Outline each Plasmodium falciparum-infected red blood cell.
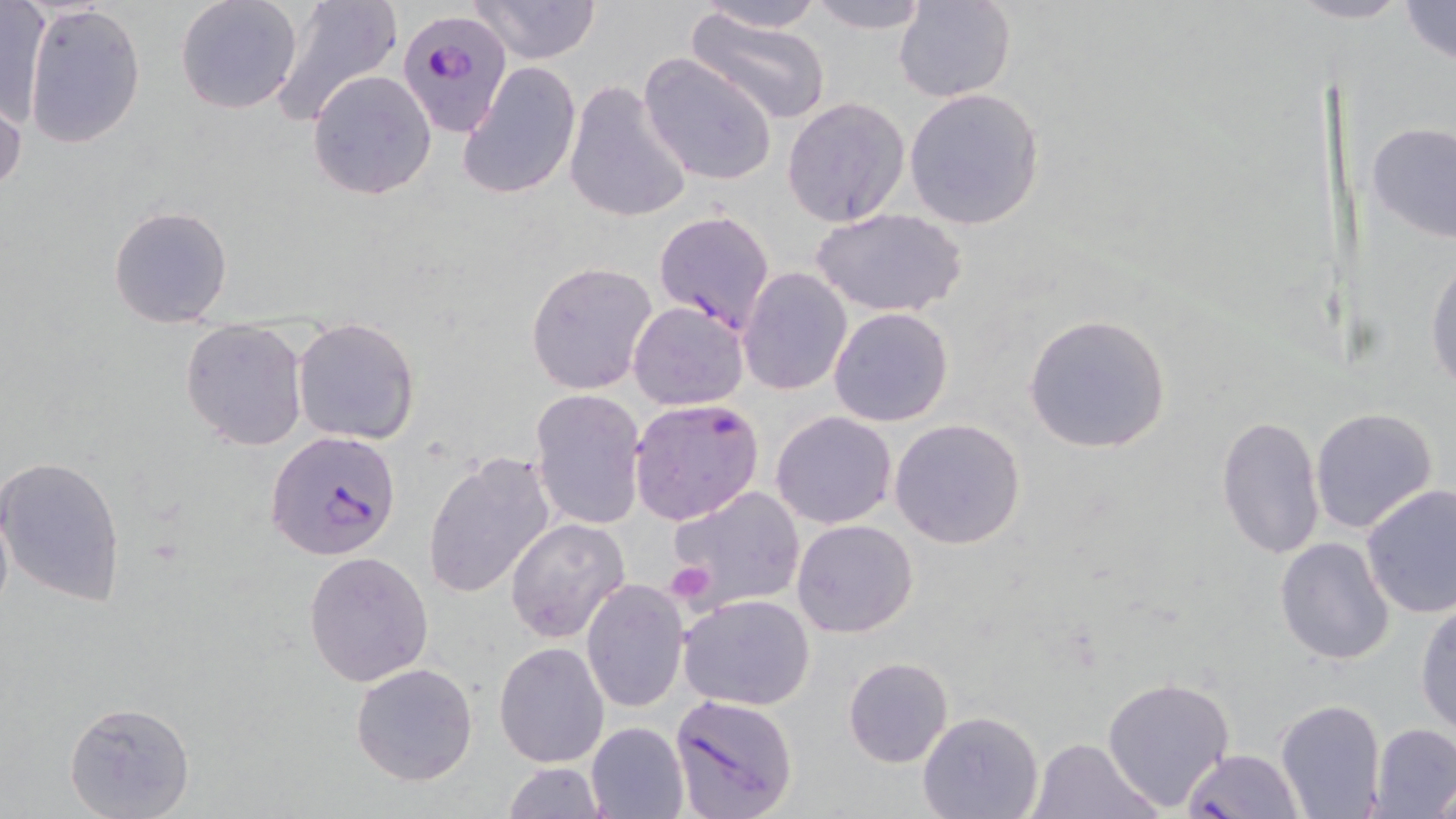

Approximate bounding boxes as (x1,y1)-(x2,y2) corner pairs in pixels.
Plasmodium falciparum-infected red blood cells: (398,5)-(513,134), (628,398)-(764,525), (266,430)-(401,561), (668,694)-(799,817), (1180,748)-(1305,819).

Summary:
  - Uninfected red blood cell locations: (1,0)-(48,128), (175,0)-(303,114), (474,0)-(600,63), (803,0)-(933,32), (895,0)-(1016,102), (1396,0)-(1455,67), (267,1)-(403,126), (691,1)-(829,34), (23,2)-(145,149), (685,10)-(833,128), (638,52)-(779,187), (457,60)-(582,201), (307,70)-(437,199), (564,80)-(693,225), (903,88)-(1044,230), (0,93)-(24,199), (782,96)-(910,227), (1366,121)-(1456,243), (108,204)-(234,329), (811,208)-(968,317), (654,209)-(775,331), (1425,250)-(1456,395), (526,261)-(656,394), (739,267)-(852,395), (629,302)-(749,411), (828,307)-(954,427), (1022,313)-(1173,455), (292,318)-(420,445), (180,320)-(307,451), (530,388)-(647,530), (1308,407)-(1438,534), (771,410)-(897,529), (1215,415)-(1326,560), (888,418)-(1027,550), (423,453)-(555,600), (0,454)-(127,605), (1360,484)-(1456,618), (669,486)-(806,609), (0,489)-(14,632), (506,516)-(631,644), (792,519)-(918,637), (1275,536)-(1394,665), (304,550)-(435,687), (581,580)-(689,713), (679,594)-(815,710), (1415,598)-(1456,737), (494,642)-(609,768), (843,657)-(952,767), (351,663)-(479,785), (1101,675)-(1236,811), (1274,699)-(1387,819), (64,700)-(195,818), (917,711)-(1042,818), (587,721)-(690,819), (1369,723)-(1455,817), (1027,736)-(1161,819), (500,762)-(607,819), (1427,778)-(1456,816)
  - Platelet locations: (666,562)-(719,607)
  - Slide-level diagnosis: Plasmodium falciparum
  - Magnification: 1000x
  - Field of view: single
  - Stain: May-Grünwald-Giemsa
  - Image size: 1456×819 pixels
  - Preparation: thin blood smear
  - Modality: light microscopy